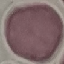

malaria_status: uninfected
preparation: thin blood film
image_type: automatically extracted cell patch, resized to 64 × 64 pixels
capture: smartphone camera at the microscope eyepiece
stain: Giemsa